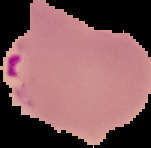 From a thin blood smear. Malaria status: parasitized. Cell region segmented out of the field of view; the surrounding area is masked to black. Image is 151×148 pixels.